Assess the morphology of the red blood cells.
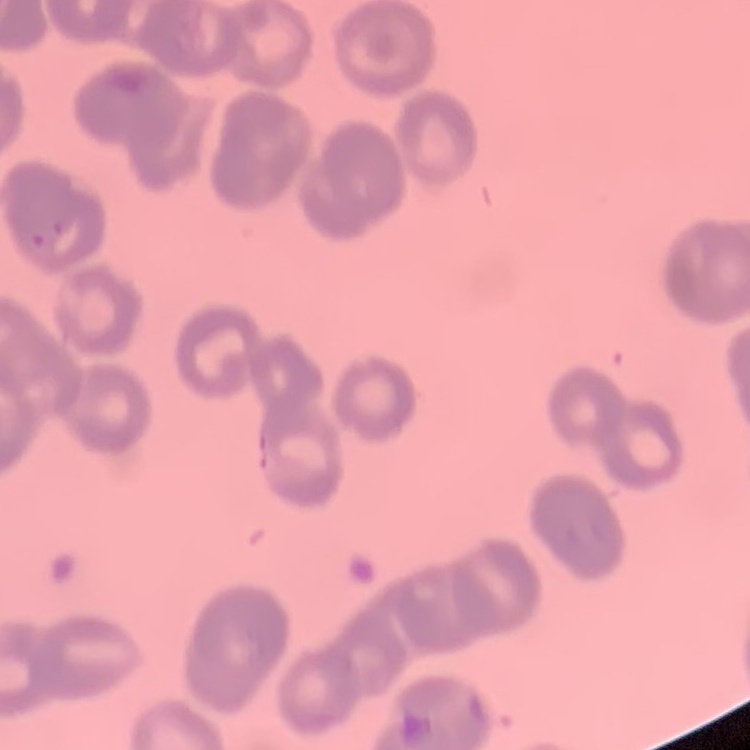

Rouleaux formation.

stain = Field's or Giemsa
preparation = thin peripheral smear
image type = square crop of a larger photomicrograph